Assess the morphology of the red blood cells.
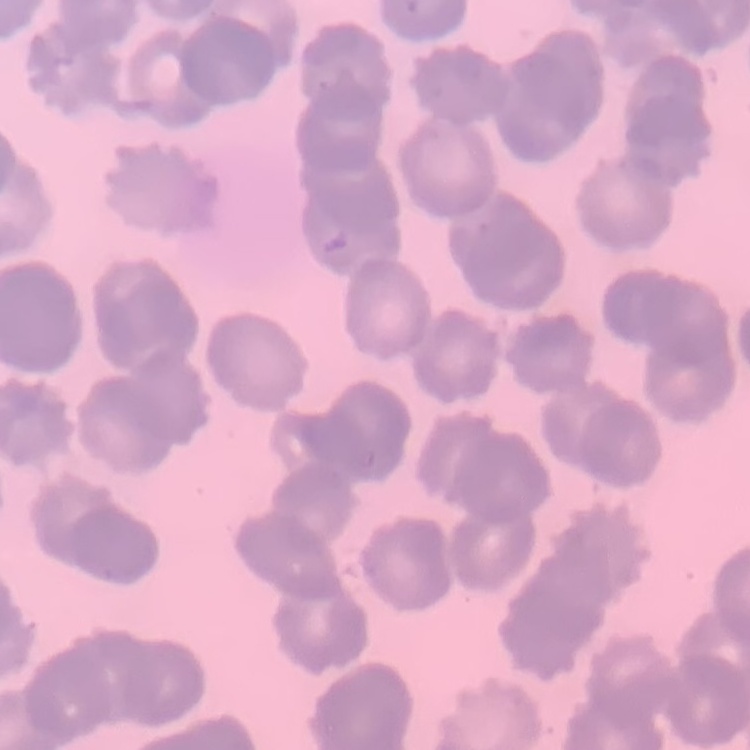
They show rouleaux formation.

Summary:
  - Image type: one tile cut from a larger photomicrograph
  - Preparation: thin blood smear
  - Stain: Field's or Giemsa